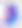

Summary:
  - Magnification: 400x
  - Modality: micrograph
  - Identification: Toxoplasma gondii